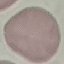

result = negative for malaria parasites
image type = automatically extracted cell patch, resized to 64 × 64 pixels
stain = Giemsa
preparation = thin blood smear
capture = smartphone camera at the microscope eyepiece